Identify the parasite.
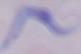
A trypanosome.

Summary:
  - Modality: micrograph
  - Magnification: 1000x